Report the malaria status of this cell.
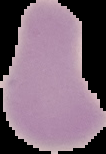

It is uninfected.

Summary:
  - Preparation: thin blood smear
  - Image type: segmented cell region with the area outside set to black
  - Image size: 106×154 pixels